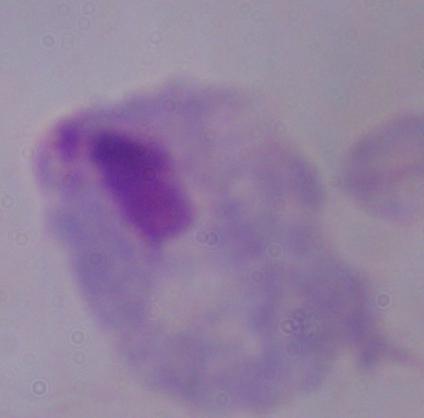
modality: micrograph
magnification: 1000x
identification: trichomonad